Outline each blood parasite and name the species.
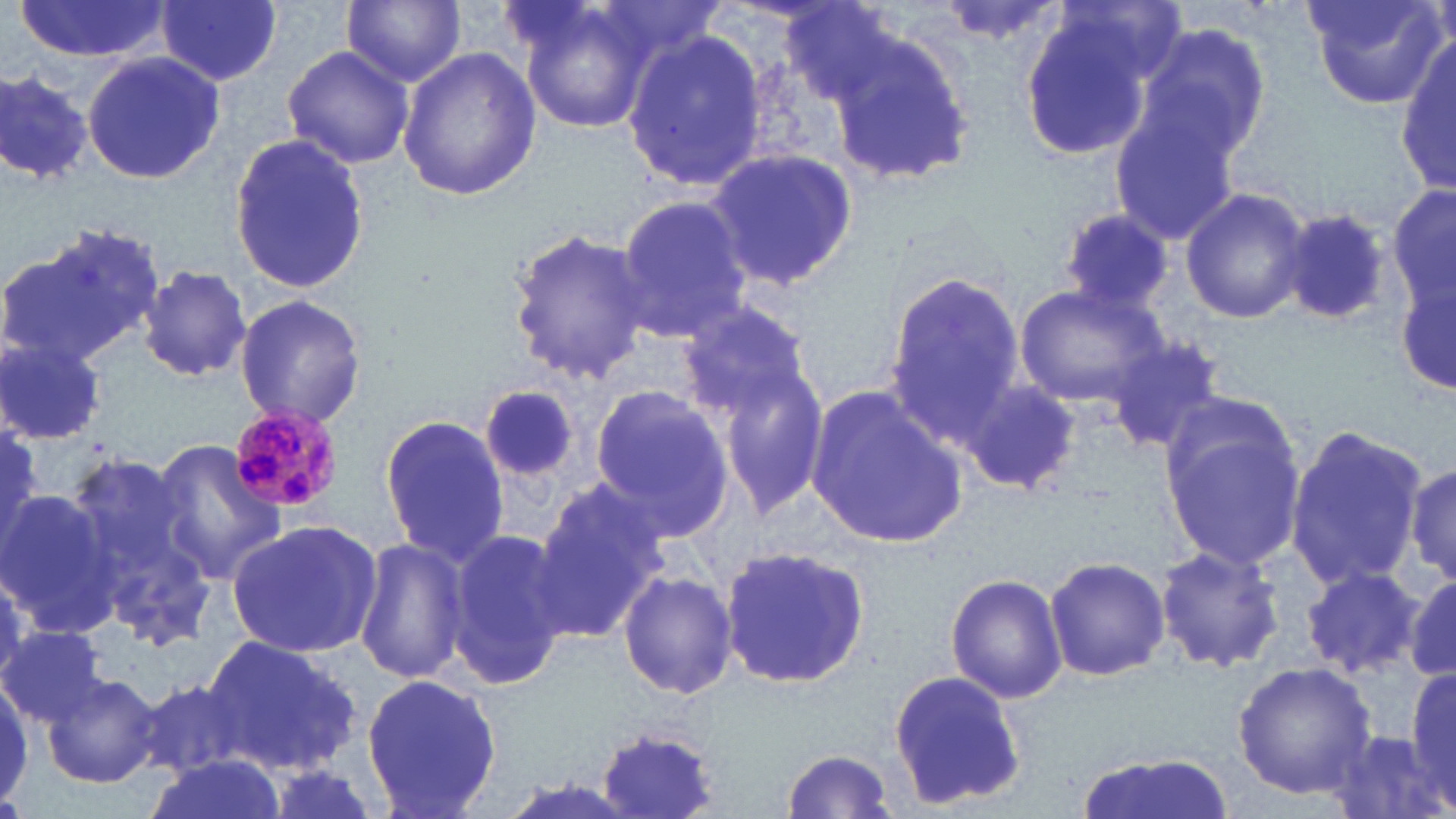

Approximate bounding boxes as named x1/y1/x2/y2 corners in pixels.
Plasmodium malariae-infected red blood cells: (x1=227, y1=404, x2=345, y2=516).
No Plasmodium falciparum, Plasmodium ovale, Plasmodium vivax, Babesia divergens, or Trypanosoma brucei observed.

Uninfected red blood cell locations: (x1=16, y1=0, x2=168, y2=60), (x1=157, y1=0, x2=283, y2=85), (x1=343, y1=0, x2=466, y2=88), (x1=510, y1=0, x2=661, y2=137), (x1=933, y1=0, x2=1069, y2=46), (x1=1305, y1=0, x2=1450, y2=111), (x1=1014, y1=10, x2=1160, y2=160), (x1=825, y1=23, x2=982, y2=188), (x1=1131, y1=24, x2=1274, y2=166), (x1=621, y1=27, x2=772, y2=195), (x1=1396, y1=38, x2=1456, y2=196), (x1=281, y1=44, x2=416, y2=171), (x1=398, y1=46, x2=541, y2=203), (x1=80, y1=51, x2=225, y2=184), (x1=0, y1=68, x2=94, y2=186), (x1=1108, y1=97, x2=1247, y2=245), (x1=227, y1=134, x2=369, y2=295), (x1=704, y1=149, x2=859, y2=291), (x1=1389, y1=180, x2=1455, y2=319), (x1=1180, y1=187, x2=1312, y2=324), (x1=614, y1=193, x2=755, y2=343), (x1=1279, y1=206, x2=1399, y2=328), (x1=1057, y1=208, x2=1175, y2=316), (x1=4, y1=223, x2=166, y2=364), (x1=504, y1=224, x2=655, y2=385), (x1=1397, y1=264, x2=1454, y2=401), (x1=137, y1=267, x2=254, y2=383), (x1=883, y1=269, x2=1026, y2=435), (x1=1013, y1=284, x2=1167, y2=409), (x1=232, y1=294, x2=368, y2=429), (x1=679, y1=295, x2=821, y2=428), (x1=0, y1=333, x2=108, y2=443), (x1=1105, y1=334, x2=1229, y2=453), (x1=714, y1=361, x2=830, y2=517), (x1=961, y1=375, x2=1083, y2=498), (x1=587, y1=384, x2=736, y2=542), (x1=804, y1=384, x2=967, y2=549), (x1=481, y1=385, x2=578, y2=486), (x1=1157, y1=405, x2=1309, y2=577), (x1=376, y1=412, x2=512, y2=566), (x1=0, y1=423, x2=46, y2=554), (x1=1284, y1=427, x2=1429, y2=594), (x1=145, y1=439, x2=287, y2=582), (x1=59, y1=446, x2=211, y2=636), (x1=1405, y1=456, x2=1456, y2=596), (x1=530, y1=480, x2=668, y2=640), (x1=0, y1=490, x2=117, y2=634), (x1=225, y1=519, x2=384, y2=658), (x1=445, y1=528, x2=573, y2=688), (x1=354, y1=536, x2=472, y2=687), (x1=1155, y1=545, x2=1284, y2=676), (x1=718, y1=546, x2=871, y2=691), (x1=1044, y1=554, x2=1172, y2=684), (x1=1299, y1=566, x2=1426, y2=681), (x1=617, y1=567, x2=737, y2=702), (x1=945, y1=573, x2=1067, y2=704), (x1=1405, y1=576, x2=1456, y2=683), (x1=0, y1=625, x2=108, y2=729), (x1=204, y1=632, x2=361, y2=776), (x1=1232, y1=660, x2=1378, y2=799), (x1=1401, y1=665, x2=1456, y2=807), (x1=886, y1=669, x2=1028, y2=810), (x1=39, y1=672, x2=165, y2=788), (x1=360, y1=672, x2=506, y2=818), (x1=0, y1=676, x2=33, y2=812), (x1=137, y1=677, x2=248, y2=779), (x1=594, y1=725, x2=725, y2=819), (x1=780, y1=749, x2=901, y2=818), (x1=1075, y1=750, x2=1237, y2=819), (x1=147, y1=756, x2=283, y2=819). Slide-level diagnosis: Plasmodium malariae. Captured at 1000x magnification. May-Grünwald-Giemsa stain. Image is 1456×819 pixels. Thin blood smear. Light microscopy. Single field of view.